Assess the morphology of the red blood cells.
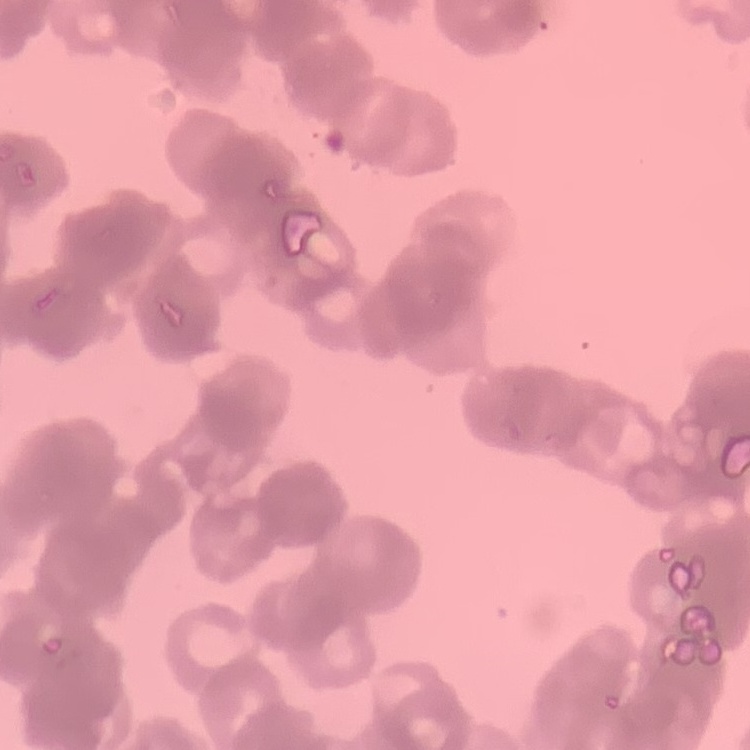
They show rouleaux formation.

Summary:
  - Stain: Field's or Giemsa
  - Preparation: thin blood smear
  - Image type: square crop of a larger photomicrograph